Locate every uninfected red blood cell.
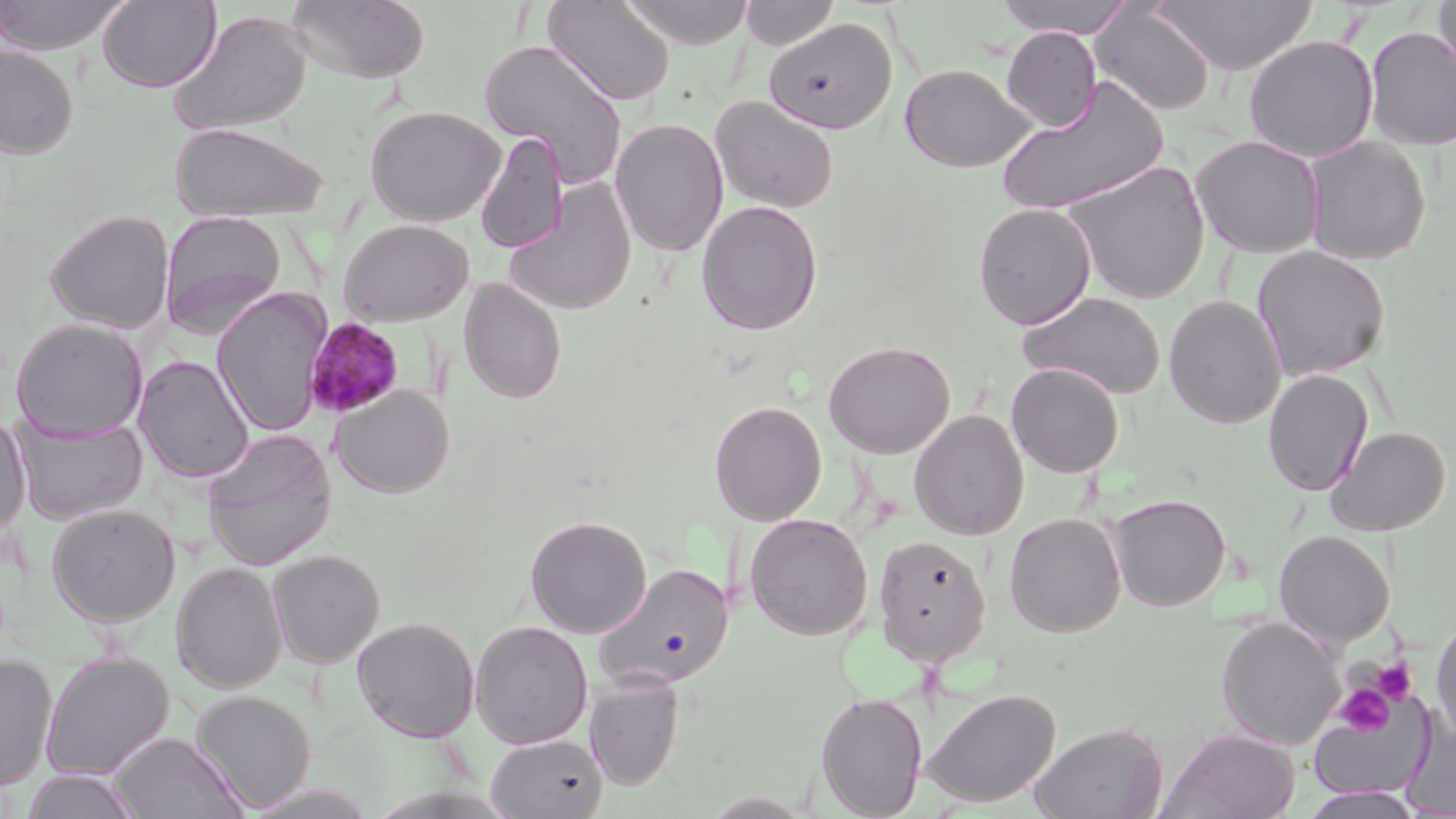
Approximate bounding boxes as [x1, y1, x2, y2] in pixels.
Uninfected red blood cells: [0, 0, 130, 54], [97, 0, 221, 92], [286, 0, 431, 83], [543, 0, 675, 106], [619, 0, 755, 48], [993, 0, 1137, 38], [1433, 0, 1456, 84], [740, 1, 841, 51], [1151, 1, 1318, 74], [1090, 3, 1216, 116], [170, 9, 311, 136], [763, 17, 897, 134], [1002, 26, 1101, 131], [1363, 27, 1456, 151], [1243, 34, 1379, 161], [479, 39, 630, 187], [0, 45, 79, 159], [899, 63, 1032, 172], [996, 77, 1169, 216], [709, 96, 839, 214], [366, 105, 505, 226], [610, 117, 729, 258], [170, 121, 329, 221], [475, 132, 569, 254], [1190, 135, 1325, 258], [1302, 135, 1432, 265], [1063, 160, 1211, 304], [505, 179, 638, 316], [696, 200, 824, 336], [973, 203, 1096, 329], [44, 209, 176, 333], [159, 209, 288, 337], [338, 219, 474, 326], [1251, 245, 1391, 381], [458, 278, 568, 404], [213, 288, 332, 436], [1018, 291, 1166, 399], [1163, 295, 1286, 428], [11, 319, 148, 439], [822, 339, 956, 459], [133, 355, 254, 483], [1006, 363, 1124, 477], [1262, 368, 1374, 496], [332, 385, 454, 498], [708, 400, 828, 526], [909, 409, 1029, 541], [0, 412, 32, 534], [13, 416, 148, 524], [1326, 426, 1451, 536], [202, 428, 337, 570], [1107, 492, 1232, 611], [46, 502, 181, 627], [744, 513, 874, 640], [1004, 513, 1126, 637], [524, 515, 652, 637], [1274, 530, 1395, 648], [872, 534, 992, 666], [267, 549, 384, 668], [171, 562, 287, 693], [594, 563, 735, 693], [352, 616, 480, 741], [1216, 616, 1344, 748], [1431, 616, 1456, 747], [471, 620, 593, 749], [39, 651, 175, 781], [0, 656, 58, 788], [584, 674, 686, 790], [922, 688, 1060, 808], [191, 690, 317, 812], [815, 690, 928, 818], [1308, 697, 1434, 800], [1031, 722, 1169, 819], [1159, 729, 1301, 819], [110, 732, 248, 819], [485, 733, 608, 818], [21, 768, 142, 819], [1299, 787, 1427, 818].

Summary:
  - Platelet locations: [1374, 658, 1416, 702], [1336, 685, 1394, 736]
  - Plasmodium malariae-infected red blood cell locations: [304, 318, 406, 419]
  - Slide-level diagnosis: Plasmodium malariae
  - Magnification: 1000x
  - Field of view: one of a larger specimen
  - Preparation: thin blood smear
  - Stain: May-Grünwald-Giemsa
  - Modality: light microscopy
  - Image size: 1456×819 pixels